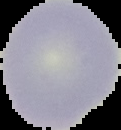
Summary:
  - Preparation: thin blood film
  - Image type: segmented cell region with the area outside set to black
  - Result: no malaria parasites seen
  - Image size: 121×130 pixels